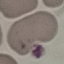
Summary:
  - Malaria status: uninfected
  - Preparation: thin blood film
  - Stain: Giemsa
  - Capture: smartphone camera at the microscope eyepiece
  - Image type: automatically extracted cell patch, resized to 64 × 64 pixels